Outline each blood parasite and name the species.
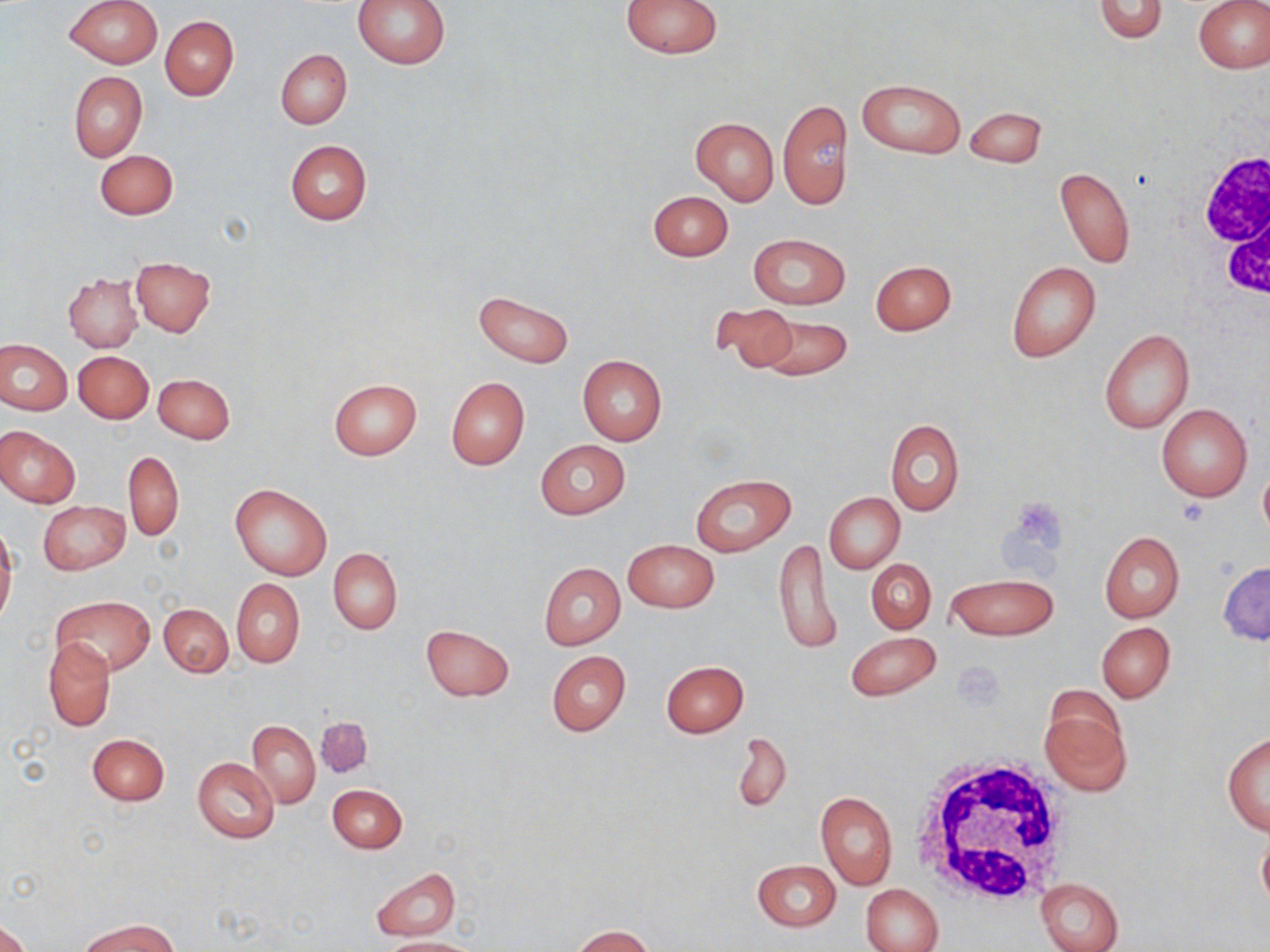

No blood parasites seen.

Summary:
  - Coordinate format: approximate bounding boxes as (x1,y1)-(x2,y2) corner pairs in pixels
  - Uninfected red blood cell locations: (65,0)-(162,68), (353,0)-(451,68), (622,0)-(723,57), (1093,0)-(1168,42), (1194,1)-(1270,72), (160,16)-(239,100), (275,50)-(351,127), (68,71)-(147,161), (857,78)-(965,158), (778,99)-(852,209), (966,107)-(1047,170), (690,116)-(778,206), (285,139)-(372,225), (95,150)-(178,219), (1054,166)-(1136,269), (647,190)-(733,262), (749,233)-(850,310), (130,257)-(216,336), (870,259)-(956,336), (1006,261)-(1100,362), (64,273)-(142,352), (474,290)-(574,368), (710,302)-(799,375), (753,314)-(852,382), (1099,329)-(1194,433), (1,339)-(71,414), (73,350)-(154,423), (577,355)-(666,446), (154,374)-(234,444), (445,377)-(530,469), (328,378)-(421,460), (1156,403)-(1253,502), (885,419)-(965,516), (0,427)-(80,507), (535,440)-(630,518), (124,450)-(183,541), (1258,459)-(1270,545), (690,473)-(796,557), (230,484)-(332,580), (823,491)-(904,573), (38,501)-(130,575), (0,529)-(17,628), (1098,530)-(1184,622), (773,537)-(840,658), (623,539)-(719,613), (329,548)-(402,635), (866,558)-(936,633), (1217,561)-(1270,644), (539,562)-(625,649), (946,573)-(1058,640), (232,579)-(304,667), (52,596)-(155,676), (159,602)-(233,677), (1096,622)-(1176,702), (420,624)-(514,702), (846,631)-(941,701), (43,638)-(115,732), (546,650)-(631,737), (661,660)-(748,737), (1040,689)-(1131,796), (247,719)-(321,808), (732,731)-(792,815), (1221,732)-(1270,834), (88,733)-(169,805), (192,756)-(279,844), (328,784)-(407,853), (816,791)-(897,890), (1256,824)-(1270,915), (751,858)-(840,932), (370,867)-(460,941), (1037,878)-(1123,952), (860,884)-(944,952), (80,919)-(177,952), (0,921)-(29,952), (571,925)-(656,952), (377,937)-(478,952)
  - White blood cell locations: (1190,140)-(1270,297), (908,753)-(1077,909)
  - Platelet locations: (953,664)-(1003,708)
  - Slide-level diagnosis: no evidence of blood parasites
  - Stain: May-Grünwald-Giemsa
  - Preparation: thin blood smear
  - Image size: 1270×952 pixels
  - Modality: light microscopy
  - Field of view: single
  - Magnification: 1000x